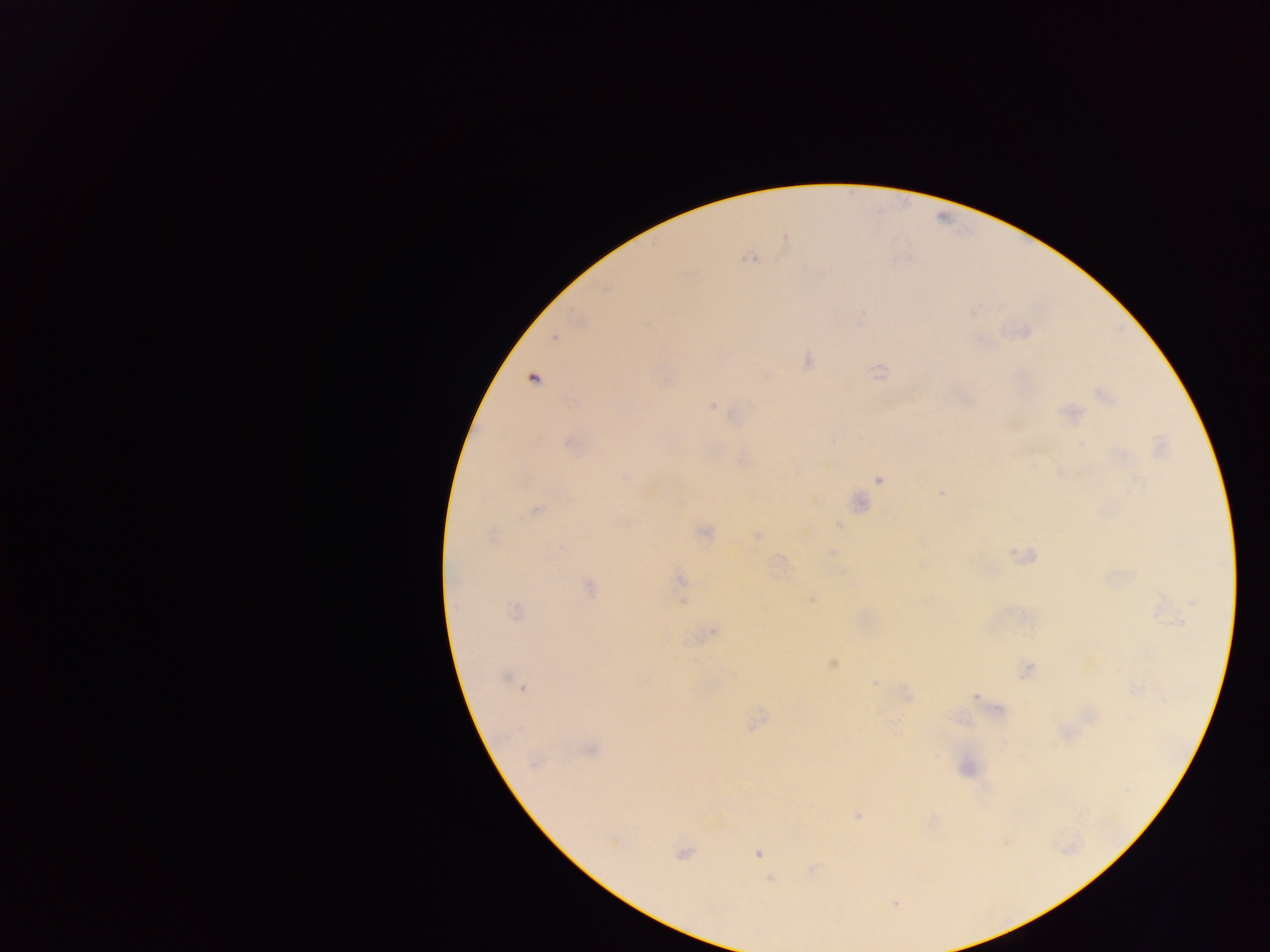

Approximate centers as {x, y} in pixels. Malaria parasite locations: {749, 258}, {554, 338}, {807, 360}, {879, 371}, {534, 380}, {665, 381}, {1104, 396}, {712, 406}, {1071, 413}, {570, 445}, {742, 460}, {624, 476}, {878, 480}, {941, 493}, {860, 503}, {537, 510}, {839, 524}, {704, 532}, {757, 535}, {492, 536}, {832, 553}, {924, 565}, {680, 579}, {589, 587}, {1193, 603}, {515, 611}, {1178, 622}, {714, 632}, {832, 664}, {1027, 670}, {733, 675}, {506, 676}, {874, 684}, {523, 688}, {975, 697}, {591, 750}, {857, 815}, {613, 842}, {682, 853}, {758, 853}, {772, 879}, {894, 904}. Thick blood smear. Photographed through a microscope with a mobile-phone camera. Image is 1270×952 pixels. Sample from Ghana. Single field of view.